State the preparation type.
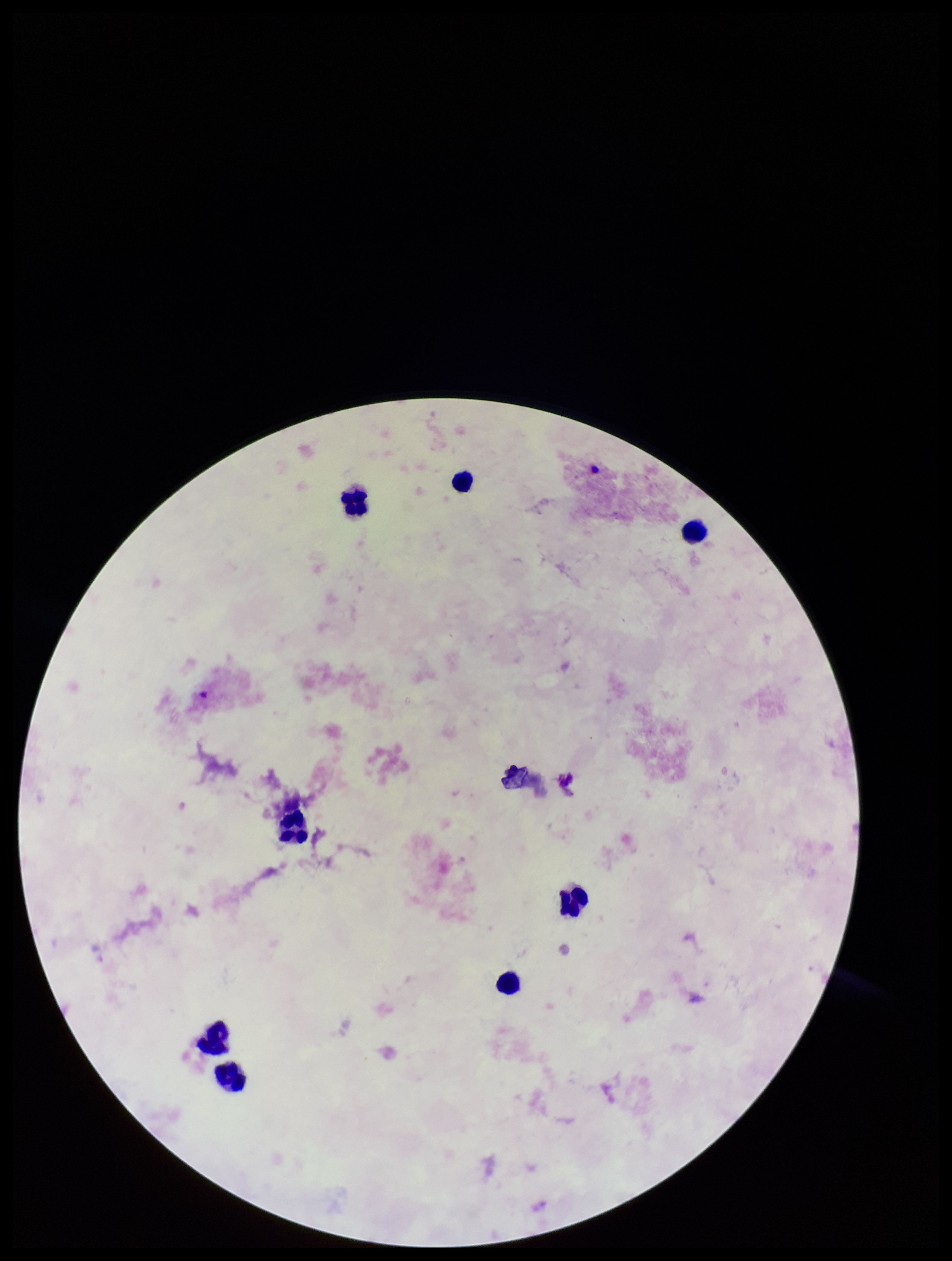
It is a thick blood smear.

{
  "capture": "smartphone photograph through the microscope eyepiece",
  "image_size": "952×1261 pixels",
  "patient_malaria_status": "negative",
  "stain": "Giemsa",
  "plasmodium_parasites": "none detected",
  "leukocyte_count": 8,
  "parasite_count": 0,
  "field_of_view": "one from this slide"
}